Outline each blood parasite and name the species.
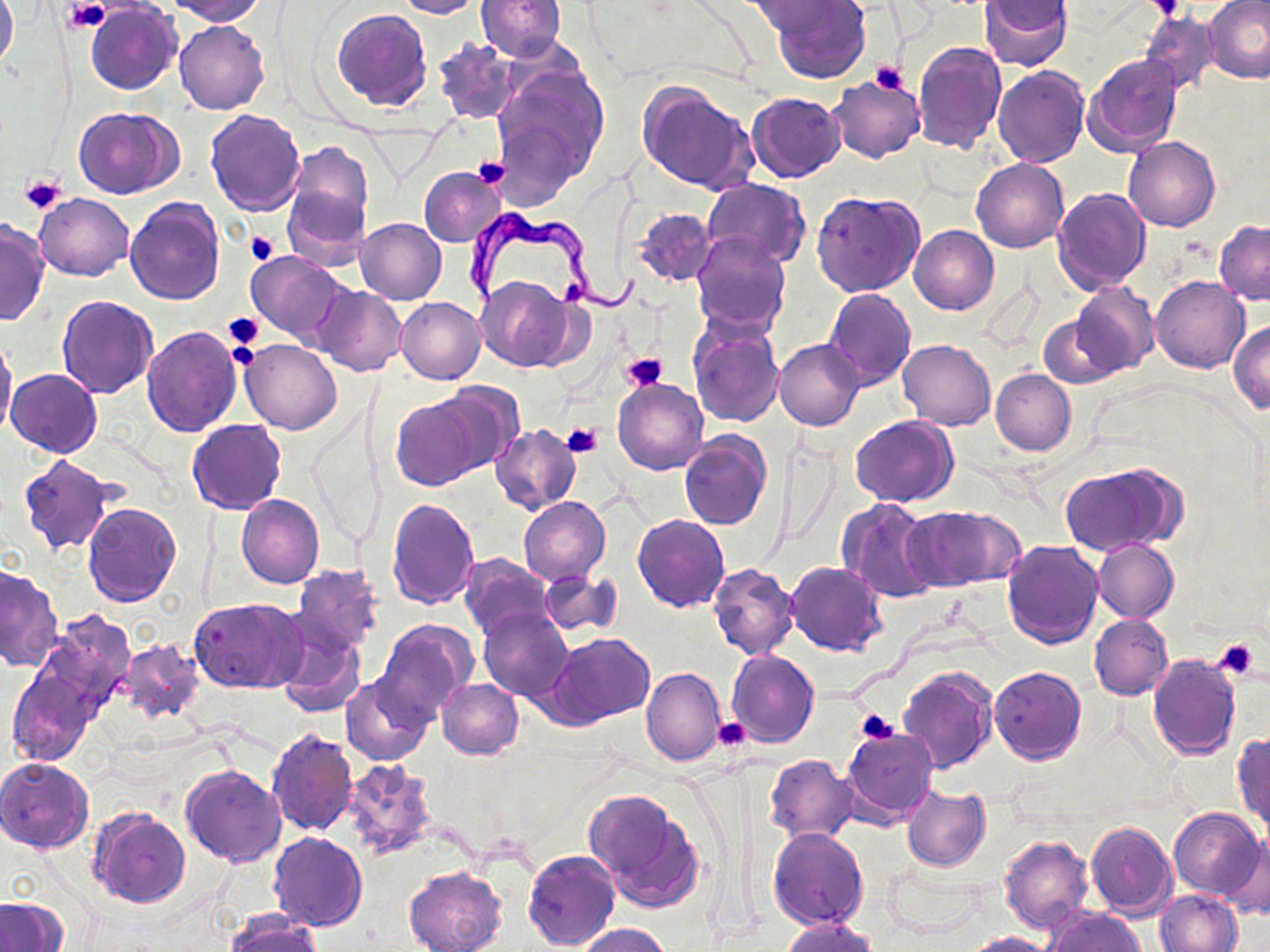
Approximate bounding boxes as (x1, y1, x2, y2) in pixels.
Trypanosoma brucei: (461, 209, 651, 320).
No Plasmodium falciparum, Plasmodium ovale, Plasmodium malariae, Plasmodium vivax, or Babesia divergens observed.

{
  "slide_level_diagnosis": "Trypanosoma brucei",
  "uninfected_red_blood_cell_locations": "approximate bounding boxes as (x1, y1, x2, y2) in pixels: (0, 0, 18, 71), (168, 0, 265, 23), (392, 0, 483, 18), (475, 0, 566, 61), (747, 0, 850, 37), (768, 0, 871, 84), (980, 1, 1073, 70), (1205, 1, 1270, 83), (86, 3, 181, 94), (332, 9, 431, 110), (1139, 10, 1221, 94), (175, 19, 269, 114), (432, 38, 521, 124), (912, 41, 1007, 154), (1083, 54, 1182, 155), (993, 66, 1089, 167), (488, 67, 608, 202), (827, 75, 924, 164), (637, 82, 760, 195), (748, 92, 844, 183), (76, 108, 181, 198), (205, 108, 306, 215), (1123, 137, 1219, 232), (286, 141, 374, 237), (972, 157, 1067, 252), (419, 167, 505, 245), (702, 180, 810, 268), (283, 184, 371, 272), (1053, 188, 1151, 293), (35, 192, 132, 281), (812, 192, 921, 297), (124, 199, 225, 305), (634, 207, 717, 287), (356, 218, 446, 303), (0, 220, 50, 325), (1214, 220, 1270, 304), (909, 226, 998, 313), (690, 231, 789, 337), (246, 251, 351, 346), (1151, 274, 1250, 373), (477, 276, 576, 370), (1070, 282, 1159, 377), (314, 286, 406, 375), (822, 288, 916, 389), (55, 294, 158, 397), (395, 297, 485, 385), (1038, 313, 1124, 387), (1230, 321, 1270, 413), (689, 323, 784, 427), (141, 326, 242, 436), (1, 335, 17, 445), (775, 338, 865, 431), (241, 339, 341, 434), (898, 340, 995, 430), (6, 369, 102, 458), (991, 369, 1076, 455), (613, 376, 707, 475), (431, 382, 525, 472), (390, 395, 484, 489), (851, 415, 957, 507), (188, 420, 286, 515), (491, 424, 580, 514), (679, 431, 771, 529), (17, 455, 118, 557), (1059, 464, 1179, 555), (238, 495, 324, 589), (520, 497, 610, 584), (837, 497, 940, 603), (386, 498, 479, 609), (82, 502, 182, 606), (908, 506, 1016, 590), (633, 514, 729, 612), (1092, 538, 1179, 622), (1002, 539, 1103, 647), (458, 554, 552, 641), (785, 561, 886, 656), (708, 563, 798, 659), (291, 564, 383, 655), (0, 566, 62, 671), (537, 571, 620, 635), (190, 598, 305, 694), (478, 606, 573, 702), (38, 611, 136, 716), (1090, 614, 1173, 700), (376, 618, 478, 722), (275, 628, 366, 718), (545, 632, 655, 726), (116, 638, 203, 723), (726, 650, 819, 747), (1147, 652, 1242, 759), (897, 664, 998, 774), (990, 666, 1086, 765), (8, 667, 95, 765), (642, 667, 725, 766), (342, 675, 434, 766), (438, 679, 523, 758), (841, 728, 938, 823), (265, 729, 358, 836), (1231, 731, 1270, 829), (765, 754, 858, 842), (0, 757, 93, 852), (339, 760, 438, 861), (180, 765, 286, 867), (902, 786, 990, 871), (585, 788, 703, 911), (89, 807, 191, 908), (1168, 807, 1264, 899), (1085, 820, 1178, 919), (768, 827, 869, 929), (269, 832, 368, 931), (1221, 834, 1270, 921), (998, 836, 1094, 934), (523, 850, 620, 950), (886, 862, 984, 936), (403, 865, 508, 952), (1155, 890, 1242, 952), (0, 897, 69, 952), (1044, 907, 1145, 952), (226, 912, 323, 952), (782, 918, 877, 952), (577, 924, 673, 952), (962, 932, 1056, 952)",
  "image_size": "1270×952 pixels",
  "platelet_locations": "approximate bounding boxes as (x1, y1, x2, y2) in pixels: (66, 0, 109, 34), (1148, 0, 1182, 22), (869, 61, 907, 93), (469, 157, 511, 190), (22, 174, 67, 216), (248, 231, 279, 266), (222, 312, 264, 350), (226, 334, 261, 373), (622, 352, 667, 390), (563, 421, 603, 456), (1213, 637, 1264, 680), (855, 708, 898, 745), (713, 718, 752, 753)",
  "preparation": "thin blood film",
  "magnification": "1000x",
  "modality": "optical microscopy",
  "stain": "May-Grünwald-Giemsa",
  "field_of_view": "single"
}